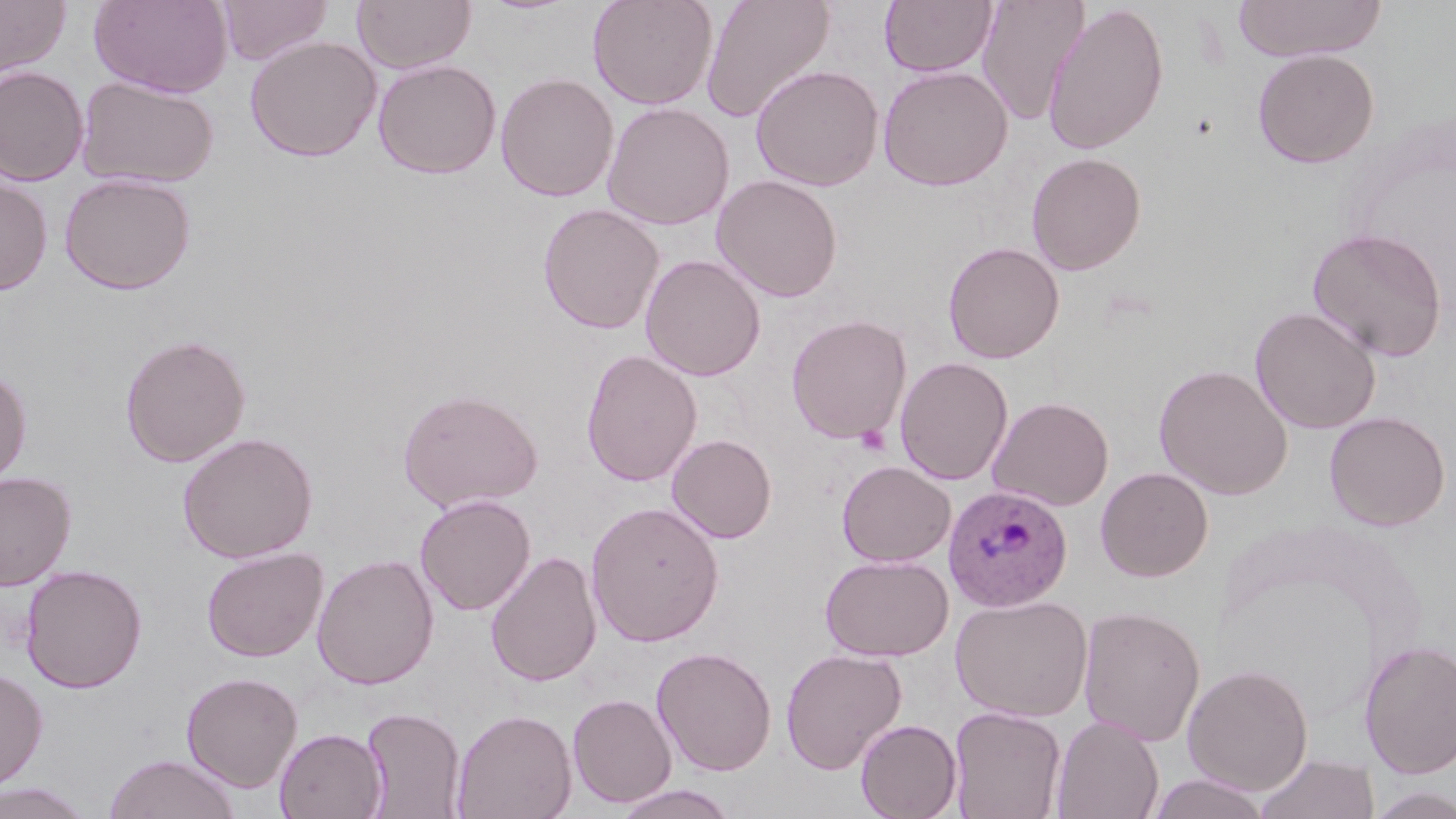

slide_level_diagnosis: Plasmodium ovale
preparation: thin blood smear
field_of_view: single
plasmodium_ovale_infected_red_blood_cell_locations: 'approximate bounding boxes as (x1, y1, x2, y2) in pixels: (943, 485, 1073, 612)'
uninfected_red_blood_cell_locations: 'approximate bounding boxes as (x1, y1, x2, y2) in pixels: (90, 0, 232, 98), (217, 0, 332, 66), (353, 0, 476, 73), (587, 0, 719, 110), (701, 0, 835, 123), (879, 0, 997, 77), (976, 0, 1090, 128), (1232, 0, 1386, 62), (0, 1, 71, 78), (1042, 2, 1170, 155), (244, 35, 381, 162), (1252, 48, 1379, 168), (373, 59, 502, 179), (750, 64, 884, 191), (877, 64, 1013, 191), (0, 66, 89, 186), (495, 71, 618, 202), (76, 75, 220, 189), (602, 101, 735, 231), (1026, 152, 1147, 275), (58, 172, 197, 294), (0, 173, 53, 296), (711, 173, 843, 303), (537, 202, 665, 335), (1307, 227, 1448, 362), (942, 241, 1065, 364), (640, 254, 766, 381), (1249, 305, 1382, 434), (786, 314, 912, 444), (119, 333, 251, 467), (581, 348, 703, 487), (894, 357, 1013, 485), (1153, 363, 1293, 500), (0, 366, 32, 487), (397, 388, 543, 512), (988, 395, 1114, 511), (1324, 410, 1450, 531), (178, 431, 318, 563), (667, 434, 777, 543), (837, 459, 956, 567), (1096, 466, 1214, 582), (0, 470, 76, 591), (414, 494, 536, 615), (585, 501, 724, 646), (200, 546, 327, 662), (486, 551, 602, 687), (312, 553, 439, 690), (819, 553, 954, 662), (20, 564, 147, 693), (950, 594, 1094, 722), (1077, 605, 1206, 746), (1359, 640, 1456, 779), (652, 645, 777, 776), (780, 647, 907, 774), (1182, 663, 1314, 795), (0, 667, 48, 792), (181, 671, 303, 792), (567, 692, 677, 808), (360, 705, 466, 819), (948, 705, 1066, 819), (451, 708, 577, 819), (1051, 715, 1164, 819), (855, 718, 962, 819), (275, 727, 387, 819), (1254, 752, 1379, 819), (104, 753, 240, 819), (1146, 773, 1272, 819), (0, 780, 96, 819), (612, 783, 739, 819), (1363, 784, 1456, 818)'
image_size: 1456×819 pixels
magnification: 1000x
modality: light microscopy
stain: May-Grünwald-Giemsa
platelet_locations: 'approximate bounding boxes as (x1, y1, x2, y2) in pixels: (855, 425, 890, 456)'